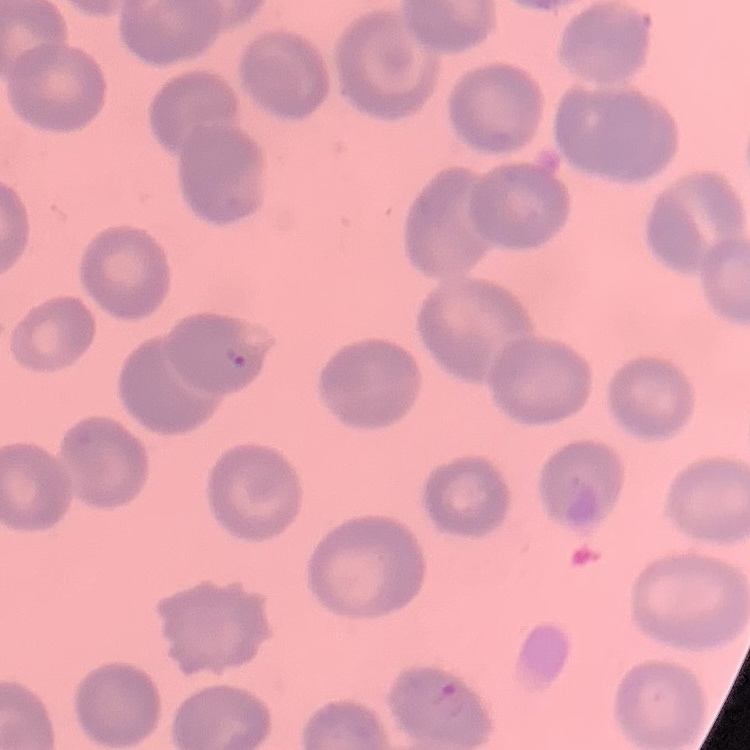

The red blood cells show no rouleaux formation. Field's or Giemsa stain. Thin peripheral smear. Square crop of a larger photomicrograph.